Give the position of every Plasmodium parasite and every leukocyte.
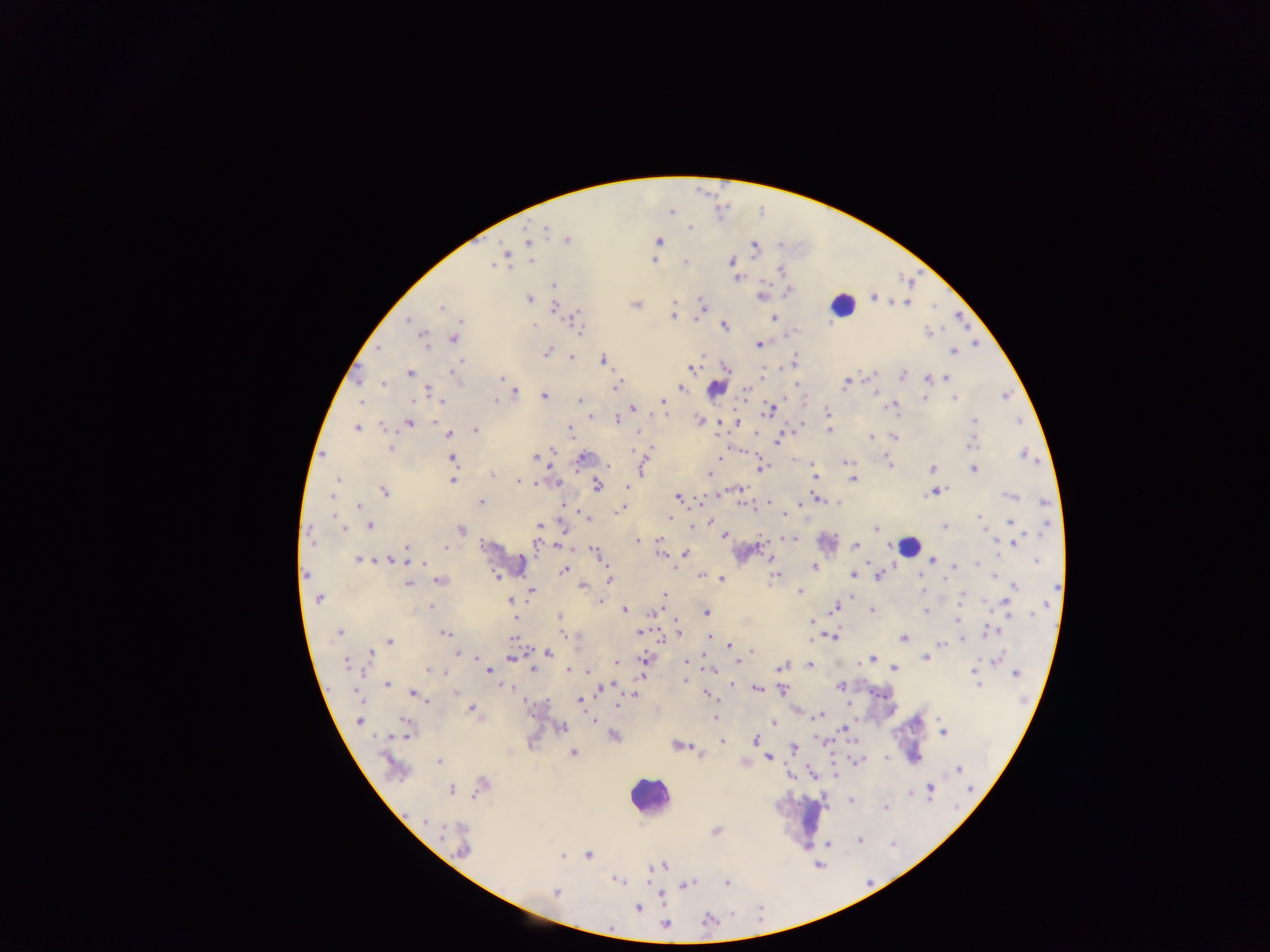

Approximate centers as (x, y) in pixels.
Plasmodium parasites: (671, 212), (690, 228), (546, 230), (568, 240), (659, 241), (528, 242), (754, 247), (504, 253), (653, 259), (530, 261), (731, 261), (685, 262), (494, 265), (781, 271), (736, 277), (554, 285), (788, 292), (874, 296), (761, 297), (529, 299), (674, 303), (908, 303), (702, 304), (636, 305), (554, 306), (441, 307), (673, 316), (576, 317), (773, 318), (408, 320), (533, 325), (724, 325), (581, 329), (928, 333), (452, 339), (424, 341), (759, 344), (379, 348), (547, 352), (954, 352), (572, 358), (603, 360), (460, 361), (693, 367), (726, 367), (410, 373), (454, 373), (873, 374), (903, 376), (947, 377), (501, 378), (929, 379), (384, 384), (844, 384), (616, 386), (680, 388), (746, 390), (429, 392), (874, 392), (515, 393), (543, 396), (1005, 396), (924, 398), (954, 398), (579, 400), (361, 401), (442, 401), (495, 401), (663, 401), (893, 406), (632, 407), (770, 410), (828, 411), (591, 417), (616, 419), (700, 420), (435, 421), (975, 421), (1019, 421), (736, 423), (409, 424), (383, 425), (356, 428), (475, 430), (829, 430), (570, 431), (448, 434), (871, 437), (894, 437), (777, 439), (972, 443), (390, 448), (651, 449), (552, 451), (633, 451), (1025, 455), (719, 457), (535, 458), (452, 459), (582, 459), (846, 462), (890, 462), (642, 467), (761, 467), (932, 468), (974, 469), (493, 475), (710, 475), (814, 476), (337, 480), (452, 480), (854, 480), (518, 482), (537, 483), (555, 483), (597, 486), (627, 486), (384, 492), (933, 493), (718, 494), (331, 495), (1011, 495), (679, 497), (819, 499), (482, 502), (1045, 502), (744, 504), (768, 504), (801, 504), (562, 505), (359, 507), (620, 510), (784, 514), (670, 517), (979, 517), (334, 518), (588, 519), (710, 522), (1010, 522), (338, 524), (370, 525), (538, 526), (693, 526), (945, 526), (343, 528), (876, 528), (1045, 528), (461, 530), (724, 536), (312, 539), (659, 539), (789, 539), (638, 541), (1015, 542), (855, 545), (446, 547), (536, 547), (558, 547), (406, 548), (596, 552), (686, 553), (661, 554), (358, 560), (933, 560), (390, 561), (1036, 562), (977, 564), (423, 565), (956, 565), (814, 568), (563, 570), (852, 574), (306, 575), (701, 575), (919, 575), (995, 575), (776, 576), (878, 576), (497, 577), (609, 579), (722, 579), (944, 580), (440, 581), (408, 585), (583, 586), (1014, 586), (1057, 588), (531, 591), (800, 591), (664, 596), (963, 596), (852, 597), (318, 599), (510, 600), (600, 602), (1006, 602), (431, 606), (835, 607), (625, 610), (872, 611), (926, 611), (654, 612), (706, 612), (1032, 615), (559, 617), (958, 619), (811, 621), (678, 631), (990, 631), (640, 632), (339, 633), (445, 634), (565, 635), (833, 636), (513, 638), (709, 638), (903, 638), (963, 640), (389, 641), (941, 643), (730, 645), (751, 651), (549, 653), (370, 654), (460, 654), (925, 657), (996, 658), (509, 659), (872, 659), (645, 660), (868, 660), (616, 662), (686, 662), (346, 663), (810, 665), (781, 666), (894, 668), (534, 669), (710, 669), (428, 670), (569, 670), (488, 671), (587, 671), (974, 672), (445, 673), (1016, 674), (685, 680), (387, 684), (977, 684), (732, 685), (840, 685), (508, 687), (757, 688), (603, 689), (783, 690), (456, 692), (357, 694), (414, 695), (635, 696), (709, 696), (579, 700), (618, 705), (471, 709), (819, 715), (715, 717), (592, 720), (359, 721), (773, 723), (562, 727), (844, 729), (407, 730), (943, 732), (613, 737), (755, 740), (722, 741), (678, 746), (794, 748), (573, 753), (767, 758), (439, 761), (959, 769), (811, 774), (837, 775), (481, 785), (931, 787), (971, 789), (451, 790), (910, 793), (850, 800), (885, 808), (425, 821), (716, 831), (859, 841), (829, 845), (462, 850), (588, 855), (562, 856), (663, 866), (616, 880), (687, 884), (726, 884), (556, 892), (638, 909), (708, 920), (664, 925).
Leukocytes: (842, 305), (717, 388), (828, 543), (909, 546), (507, 560), (648, 796), (810, 815).

Summary:
  - Field of view: single
  - Country: Ghana
  - Capture: mobile-phone photograph through a microscope
  - Preparation: thick blood film
  - Image size: 1270×952 pixels